Classify this cell by malaria status.
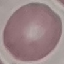

It is uninfected.

Summary:
  - Image type: cell patch, automatically extracted from a larger field of view and resized to 64 × 64 pixels
  - Stain: Giemsa
  - Capture: smartphone camera at the microscope eyepiece
  - Preparation: thin blood smear